Name the parasite shown.
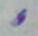

This is Toxoplasma gondii.

magnification = 1000x
modality = photomicrograph